Assess this cell for malaria.
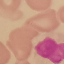
It is uninfected.

Summary:
  - Preparation: thin blood film
  - Stain: Giemsa
  - Image type: automatically extracted cell patch, resized to 64 × 64 pixels
  - Capture: smartphone through the microscope eyepiece